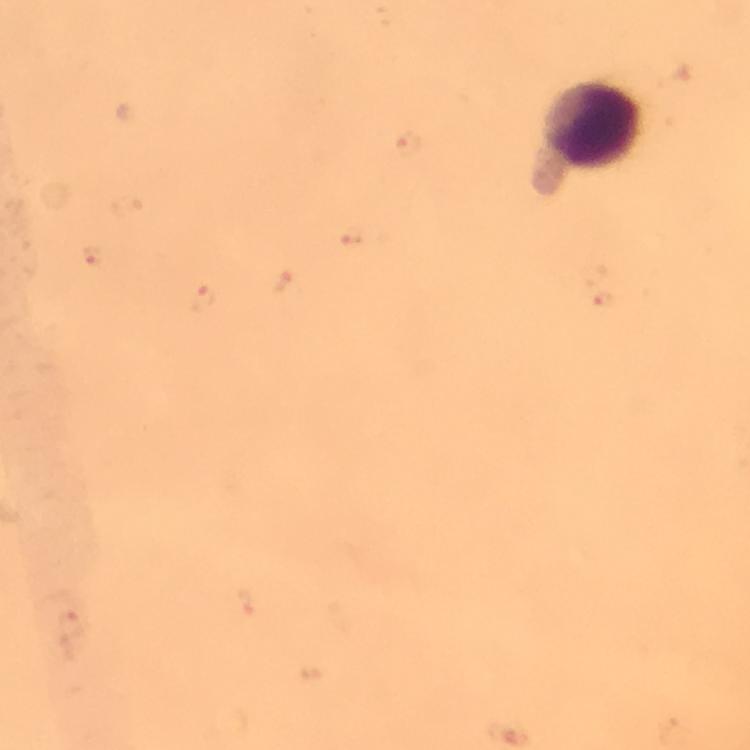

Approximate centers as (x, y) in pixels. Malaria parasite locations: (409, 145), (352, 238), (90, 257), (283, 285), (201, 298), (603, 299), (248, 602), (73, 626). Leukocyte locations: (593, 127). Smartphone photograph taken through a microscope. From a diagnostic examination for malaria. 100x magnification. Image is 750×750 pixels. Giemsa stain. Immersion oil was used. Thick blood film. Cropped region of a single field of view.